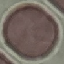 Malaria status: uninfected. Automatically extracted cell patch, resized to 64 × 64 pixels. Thin blood smear. Acquired by smartphone through the microscope eyepiece. Giemsa stain.